Assess the morphology of the erythrocytes.
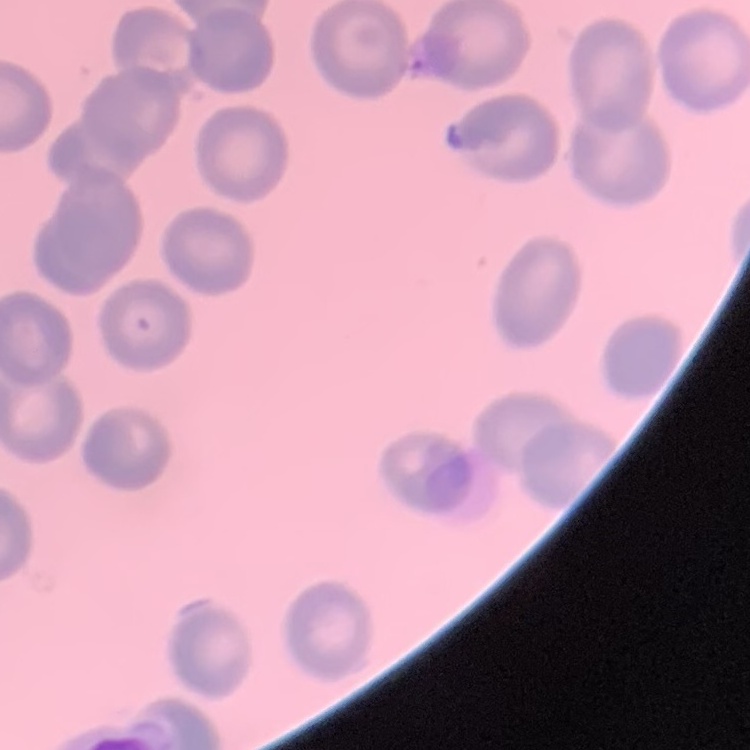
They show no rouleaux formation.

Summary:
  - Stain: Field's or Giemsa
  - Preparation: thin blood film
  - Image type: square crop of a larger photomicrograph